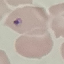

Summary:
  - Result: malaria parasites identified
  - Capture: smartphone camera at the microscope eyepiece
  - Image type: cell patch, automatically extracted from a larger field of view and resized to 64 × 64 pixels
  - Preparation: thin blood smear
  - Stain: Giemsa